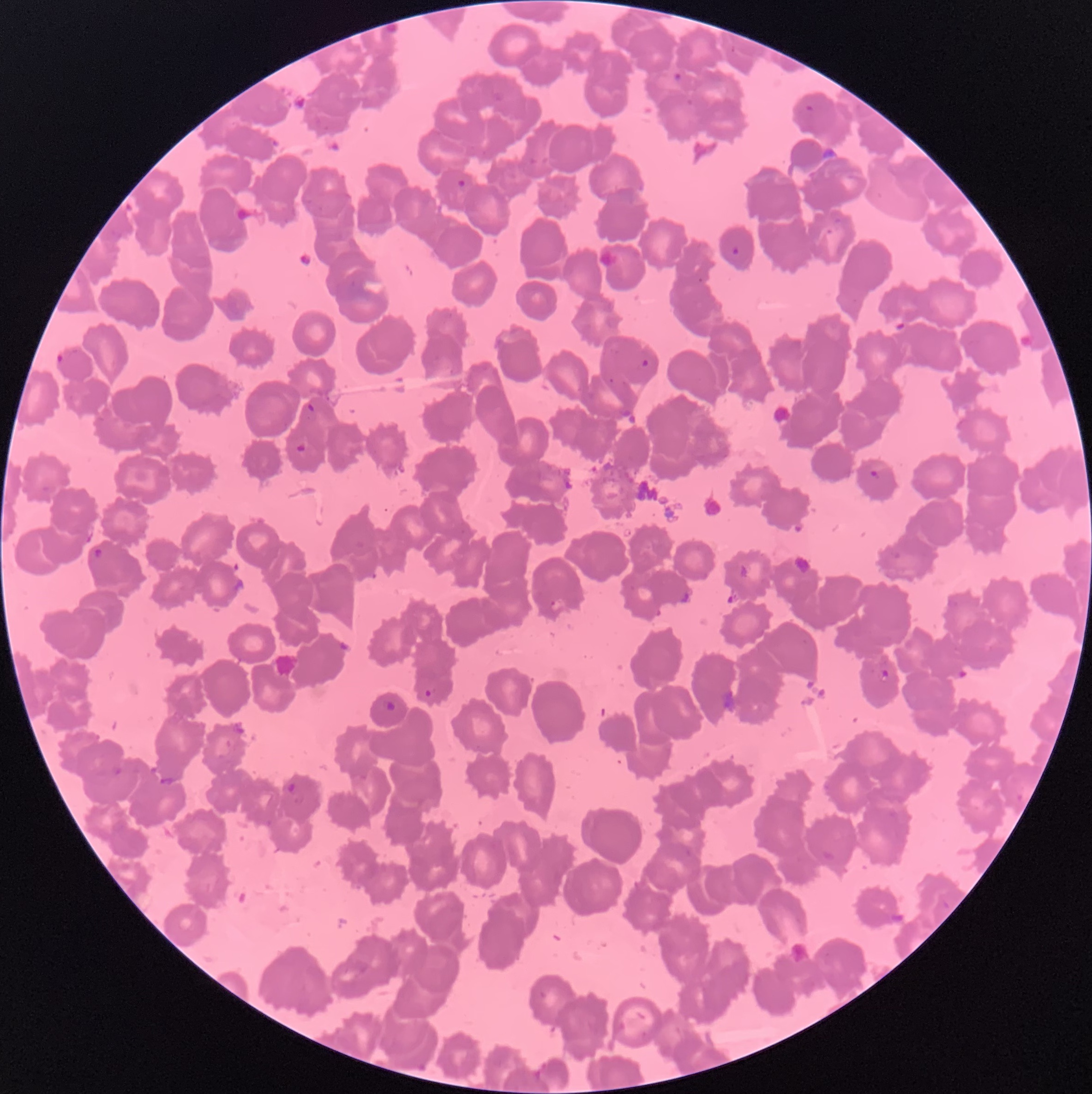

Summary:
  - Coordinate format: approximate bounding boxes as [x1, y1, x2, y2] in pixels
  - Plasmodium parasite locations: [671, 71, 685, 83], [806, 105, 814, 111], [454, 178, 468, 191], [729, 245, 742, 260], [57, 353, 65, 364], [639, 357, 651, 371], [303, 401, 317, 415], [292, 442, 310, 456], [870, 469, 881, 480], [90, 545, 106, 561], [549, 598, 566, 611], [879, 668, 891, 683], [422, 688, 435, 699], [284, 780, 298, 796]
  - Image size: 1092×1094 pixels
  - Red blood cell morphology: rouleaux formation
  - Preparation: thin blood film
  - Modality: optical microscopy